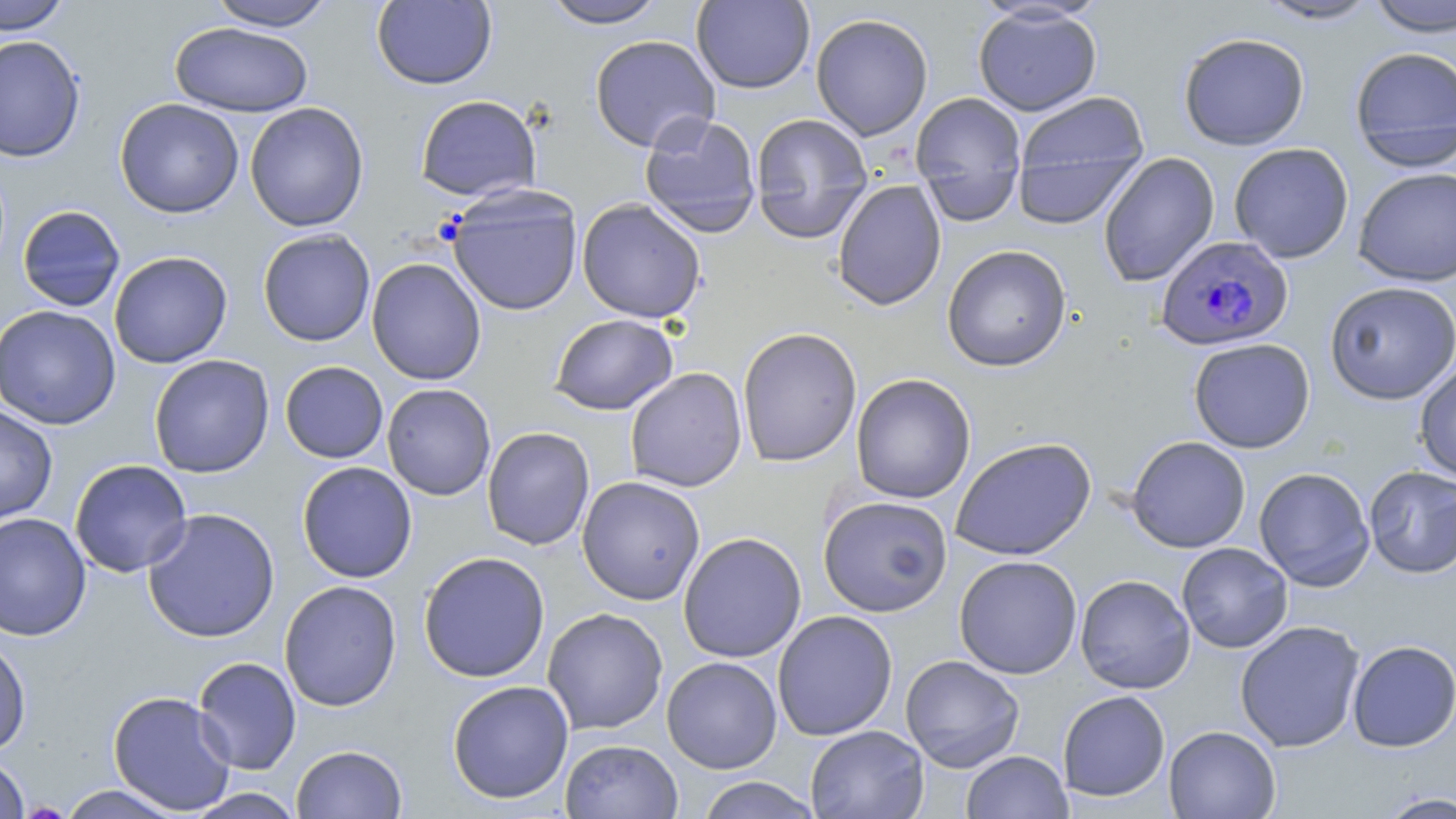
slide_level_diagnosis: Plasmodium falciparum
preparation: thin blood film
image_size: 1456×819 pixels
stain: May-Grünwald-Giemsa
plasmodium_falciparum_infected_red_blood_cell_locations: 'approximate bounding boxes as [x1, y1, x2, y2] in pixels: [1155, 235, 1294, 350]'
modality: optical microscopy
field_of_view: one of a larger specimen
uninfected_red_blood_cell_locations: 'approximate bounding boxes as [x1, y1, x2, y2] in pixels: [0, 0, 71, 35], [541, 0, 669, 29], [1254, 0, 1382, 24], [1365, 0, 1456, 37], [206, 1, 337, 31], [372, 1, 497, 89], [691, 1, 815, 94], [973, 5, 1102, 116], [811, 13, 933, 140], [169, 22, 313, 117], [1178, 32, 1310, 151], [589, 34, 720, 152], [0, 35, 85, 162], [1349, 46, 1456, 168], [910, 91, 1028, 222], [1013, 91, 1150, 221], [414, 95, 542, 202], [114, 98, 244, 218], [245, 102, 369, 232], [638, 112, 762, 238], [750, 112, 873, 243], [1228, 142, 1354, 263], [1098, 152, 1219, 287], [1352, 168, 1456, 286], [832, 179, 947, 311], [446, 187, 583, 316], [576, 198, 706, 323], [17, 205, 125, 311], [258, 228, 376, 347], [942, 244, 1072, 372], [108, 251, 233, 369], [366, 257, 487, 385], [1324, 281, 1456, 404], [0, 304, 121, 430], [549, 313, 679, 415], [736, 327, 862, 467], [1188, 337, 1316, 453], [149, 355, 275, 478], [1414, 359, 1456, 485], [280, 361, 388, 463], [625, 367, 747, 492], [851, 373, 976, 504], [382, 383, 496, 501], [0, 404, 58, 525], [481, 426, 595, 551], [1126, 436, 1251, 553], [950, 437, 1096, 561], [69, 459, 193, 577], [297, 461, 417, 583], [1363, 466, 1456, 578], [1253, 467, 1376, 591], [577, 476, 705, 605], [818, 495, 953, 617], [142, 508, 280, 644], [0, 512, 91, 641], [678, 532, 806, 662], [1176, 542, 1293, 653], [418, 551, 550, 683], [953, 555, 1083, 679], [1075, 574, 1195, 694], [279, 580, 402, 712], [542, 608, 669, 735], [772, 610, 898, 741], [1235, 620, 1365, 753], [0, 635, 32, 758], [1346, 640, 1456, 752], [900, 655, 1025, 772], [661, 656, 782, 774], [192, 657, 302, 774], [447, 680, 574, 804], [107, 690, 237, 815], [1058, 690, 1170, 802], [805, 725, 929, 819], [1163, 725, 1281, 818], [560, 738, 683, 819], [291, 744, 408, 819], [961, 750, 1072, 818], [0, 755, 30, 818], [695, 776, 823, 818], [57, 785, 184, 818], [183, 788, 306, 818], [1377, 791, 1456, 818]'
magnification: 1000x